Assess the morphology of the red blood cells.
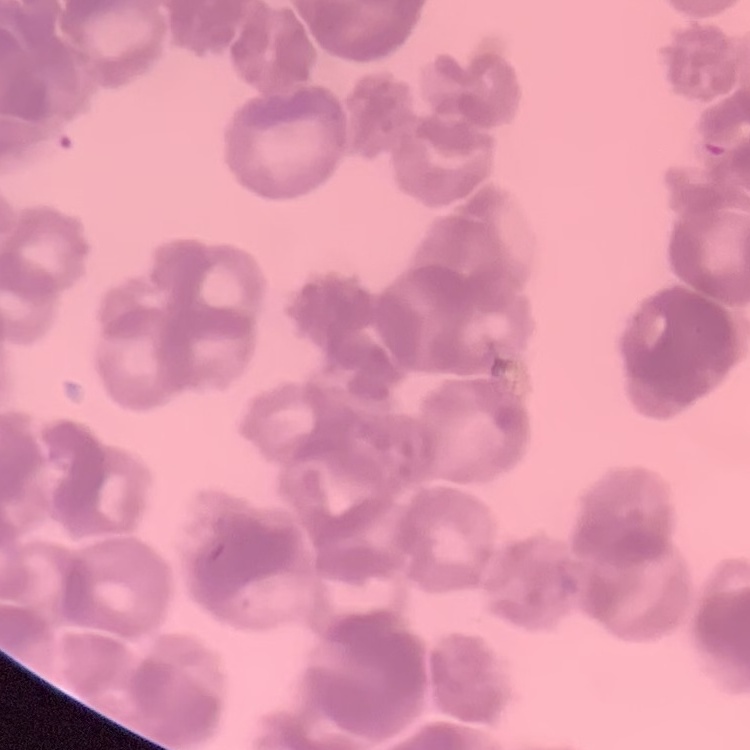
Rouleaux formation.

Field's or Giemsa stain. Square crop of a larger photomicrograph. Thin blood smear.